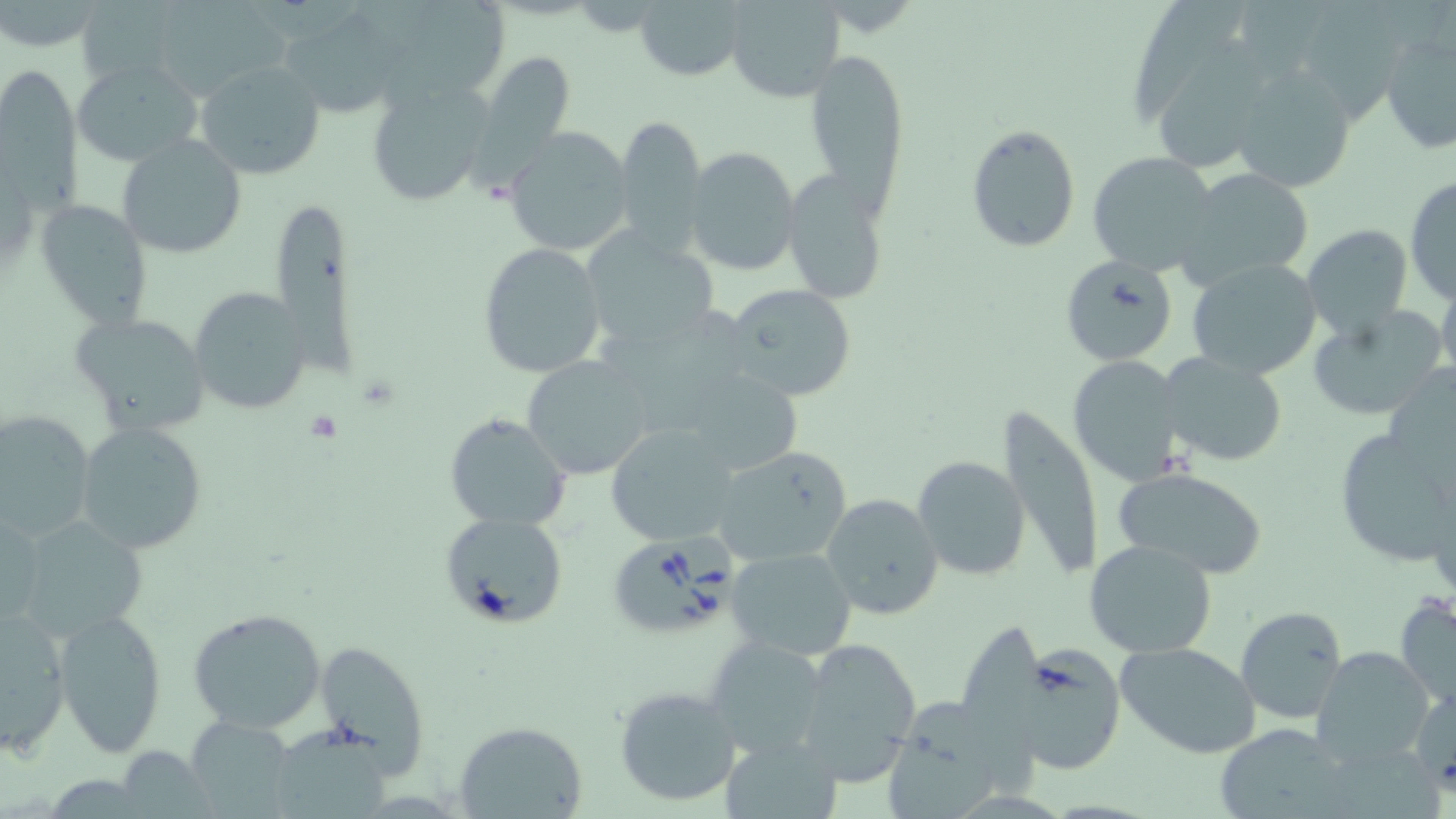

Approximate bounding boxes as named x1/y1/x2/y2 corners in pixels. Uninfected red blood cell locations: (x1=85, y1=0, x2=187, y2=78), (x1=418, y1=0, x2=508, y2=88), (x1=1308, y1=0, x2=1411, y2=132), (x1=164, y1=1, x2=290, y2=101), (x1=635, y1=1, x2=748, y2=82), (x1=724, y1=1, x2=845, y2=102), (x1=1135, y1=1, x2=1245, y2=127), (x1=287, y1=11, x2=392, y2=113), (x1=1379, y1=25, x2=1456, y2=157), (x1=1160, y1=35, x2=1266, y2=171), (x1=472, y1=47, x2=577, y2=179), (x1=807, y1=51, x2=909, y2=205), (x1=71, y1=59, x2=201, y2=167), (x1=196, y1=60, x2=327, y2=180), (x1=1228, y1=64, x2=1357, y2=193), (x1=1, y1=70, x2=79, y2=215), (x1=363, y1=76, x2=495, y2=208), (x1=616, y1=114, x2=706, y2=256), (x1=965, y1=124, x2=1081, y2=253), (x1=504, y1=126, x2=633, y2=258), (x1=116, y1=135, x2=249, y2=259), (x1=684, y1=148, x2=799, y2=278), (x1=1085, y1=152, x2=1219, y2=277), (x1=1175, y1=167, x2=1316, y2=291), (x1=781, y1=174, x2=887, y2=305), (x1=1404, y1=175, x2=1456, y2=304), (x1=35, y1=197, x2=153, y2=333), (x1=273, y1=203, x2=355, y2=372), (x1=1301, y1=224, x2=1413, y2=344), (x1=580, y1=231, x2=719, y2=353), (x1=477, y1=243, x2=607, y2=378), (x1=1058, y1=254, x2=1179, y2=365), (x1=1187, y1=258, x2=1323, y2=381), (x1=1435, y1=283, x2=1456, y2=382), (x1=723, y1=284, x2=858, y2=403), (x1=188, y1=287, x2=309, y2=414), (x1=1308, y1=308, x2=1443, y2=421), (x1=70, y1=311, x2=211, y2=436), (x1=598, y1=333, x2=748, y2=437), (x1=1159, y1=350, x2=1287, y2=467), (x1=1067, y1=355, x2=1184, y2=485), (x1=522, y1=356, x2=655, y2=481), (x1=693, y1=374, x2=804, y2=474), (x1=993, y1=405, x2=1104, y2=583), (x1=0, y1=410, x2=97, y2=545), (x1=444, y1=412, x2=572, y2=529), (x1=74, y1=423, x2=206, y2=553), (x1=604, y1=424, x2=743, y2=548), (x1=1338, y1=435, x2=1452, y2=564), (x1=708, y1=445, x2=855, y2=566), (x1=912, y1=455, x2=1031, y2=581), (x1=1113, y1=466, x2=1269, y2=579), (x1=821, y1=492, x2=946, y2=623), (x1=1, y1=504, x2=44, y2=635), (x1=438, y1=511, x2=569, y2=631), (x1=12, y1=515, x2=152, y2=645), (x1=1085, y1=538, x2=1218, y2=658), (x1=725, y1=546, x2=857, y2=662), (x1=1394, y1=593, x2=1456, y2=712), (x1=52, y1=605, x2=169, y2=759), (x1=186, y1=605, x2=330, y2=735), (x1=1235, y1=605, x2=1348, y2=723), (x1=1, y1=608, x2=72, y2=754), (x1=959, y1=624, x2=1043, y2=796), (x1=791, y1=634, x2=922, y2=786), (x1=704, y1=635, x2=830, y2=758), (x1=316, y1=638, x2=429, y2=772), (x1=1115, y1=641, x2=1263, y2=758), (x1=1008, y1=643, x2=1124, y2=775), (x1=1310, y1=645, x2=1433, y2=768), (x1=613, y1=686, x2=743, y2=807), (x1=1409, y1=686, x2=1456, y2=791), (x1=888, y1=697, x2=999, y2=819), (x1=188, y1=714, x2=296, y2=819), (x1=453, y1=720, x2=586, y2=818), (x1=1211, y1=723, x2=1355, y2=819), (x1=280, y1=726, x2=387, y2=819), (x1=724, y1=734, x2=838, y2=818), (x1=1336, y1=747, x2=1444, y2=819), (x1=121, y1=750, x2=220, y2=819). Babesia divergens-infected red blood cell locations: (x1=610, y1=532, x2=738, y2=633). Slide-level diagnosis: Babesia divergens. Image is 1456×819 pixels. Light microscopy. Thin blood film. 1000x magnification. May-Grünwald-Giemsa stain. One field of a larger specimen.